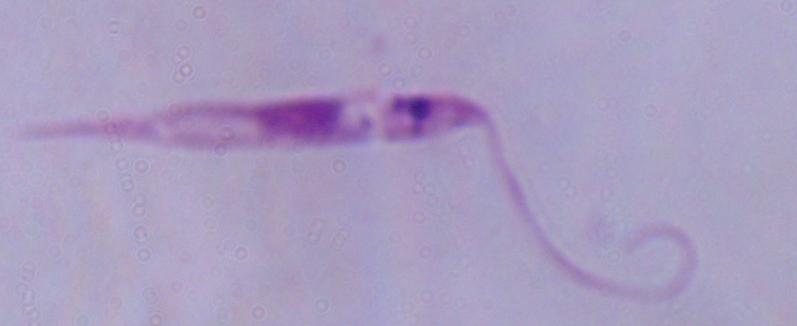

identification = Leishmania
magnification = 1000x
modality = photomicrograph